Identify the parasite.
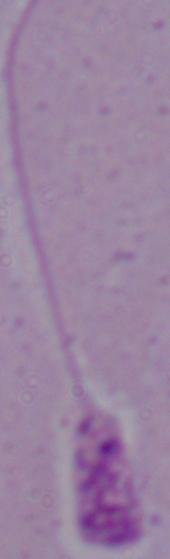

Leishmania.

magnification = 1000x
modality = photomicrograph